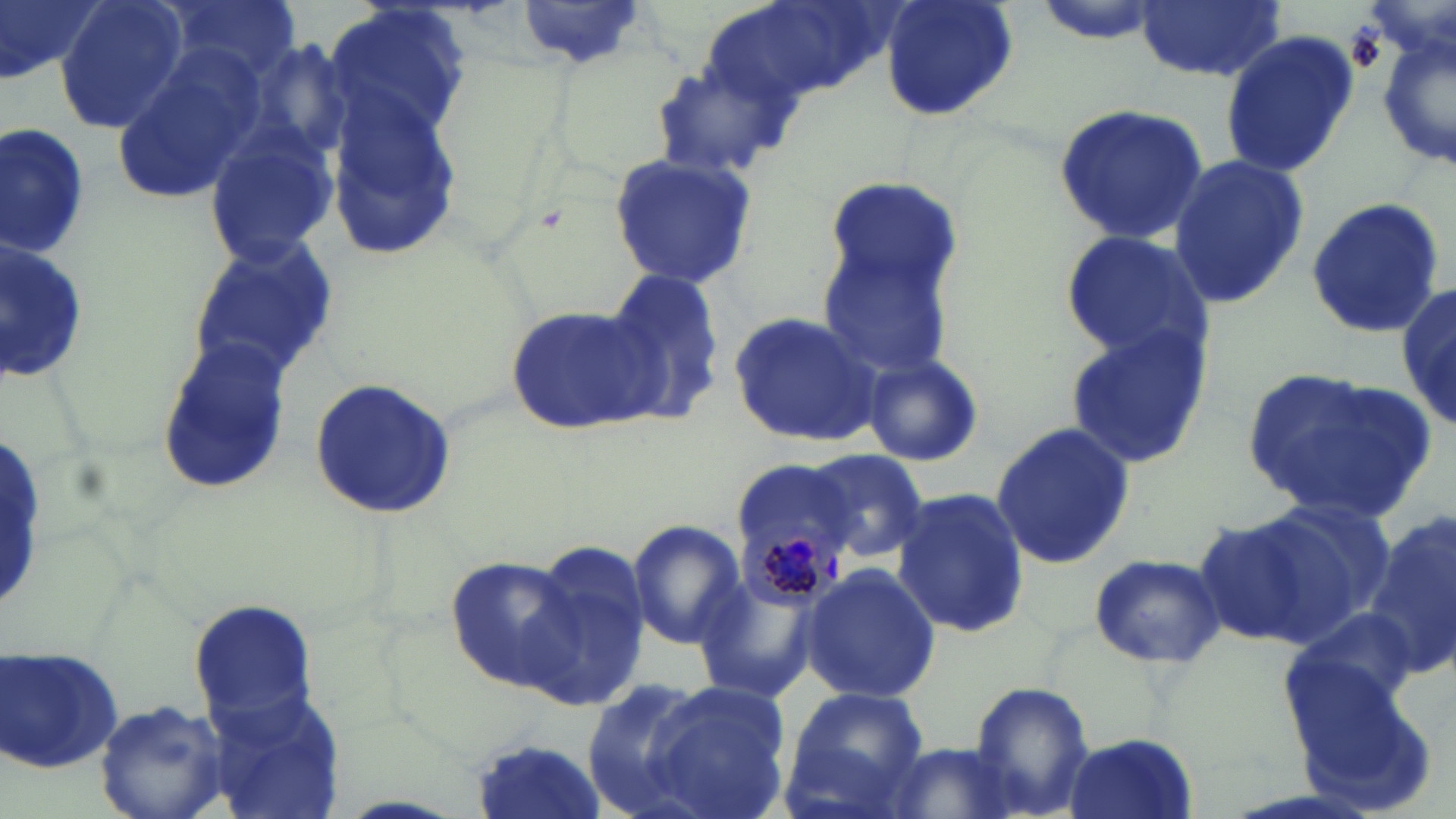
Approximate bounding boxes as (x1, y1, x2, y2) in pixels. Uninfected red blood cell locations: (0, 0, 101, 88), (53, 0, 190, 136), (161, 0, 300, 83), (703, 0, 889, 115), (879, 0, 1019, 124), (1135, 0, 1283, 83), (322, 1, 473, 146), (516, 2, 652, 72), (1376, 30, 1453, 176), (1220, 31, 1357, 174), (112, 41, 268, 201), (649, 57, 797, 180), (325, 95, 459, 261), (1053, 102, 1210, 245), (0, 126, 90, 260), (202, 127, 337, 266), (1166, 151, 1311, 307), (606, 152, 760, 292), (821, 175, 961, 310), (1304, 199, 1445, 337), (1057, 228, 1211, 367), (186, 235, 338, 384), (0, 239, 91, 386), (816, 245, 957, 375), (603, 269, 729, 423), (1397, 276, 1454, 437), (505, 299, 665, 436), (729, 309, 885, 449), (1062, 325, 1212, 469), (154, 337, 292, 493), (858, 352, 983, 467), (1240, 368, 1436, 520), (306, 378, 457, 519), (989, 421, 1135, 569), (799, 448, 931, 562), (729, 461, 858, 544), (891, 489, 1028, 640), (1252, 499, 1393, 640), (1191, 513, 1333, 649), (1363, 513, 1456, 682), (624, 519, 744, 649), (526, 540, 654, 703), (1088, 551, 1223, 670), (445, 555, 586, 692), (799, 563, 942, 703), (691, 575, 819, 705), (186, 598, 320, 727), (1286, 601, 1423, 715), (2, 645, 126, 778), (576, 676, 710, 812), (968, 680, 1095, 819), (644, 682, 788, 818), (199, 685, 352, 819), (779, 687, 931, 813), (95, 700, 235, 819), (1063, 734, 1199, 819), (468, 736, 609, 819), (880, 742, 1025, 818). Plasmodium malariae-infected red blood cell locations: (734, 512, 845, 619). Slide-level diagnosis: Plasmodium malariae. Image is 1456×819 pixels. Thin blood smear. Single field of view. May-Grünwald-Giemsa stain. Optical microscopy. 1000x magnification.